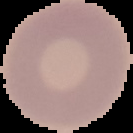

Result: no malaria parasites seen. The area outside the segmented cell region is set to black. Image is 133×133 pixels. From a thin blood smear.